Point out each leukocyte.
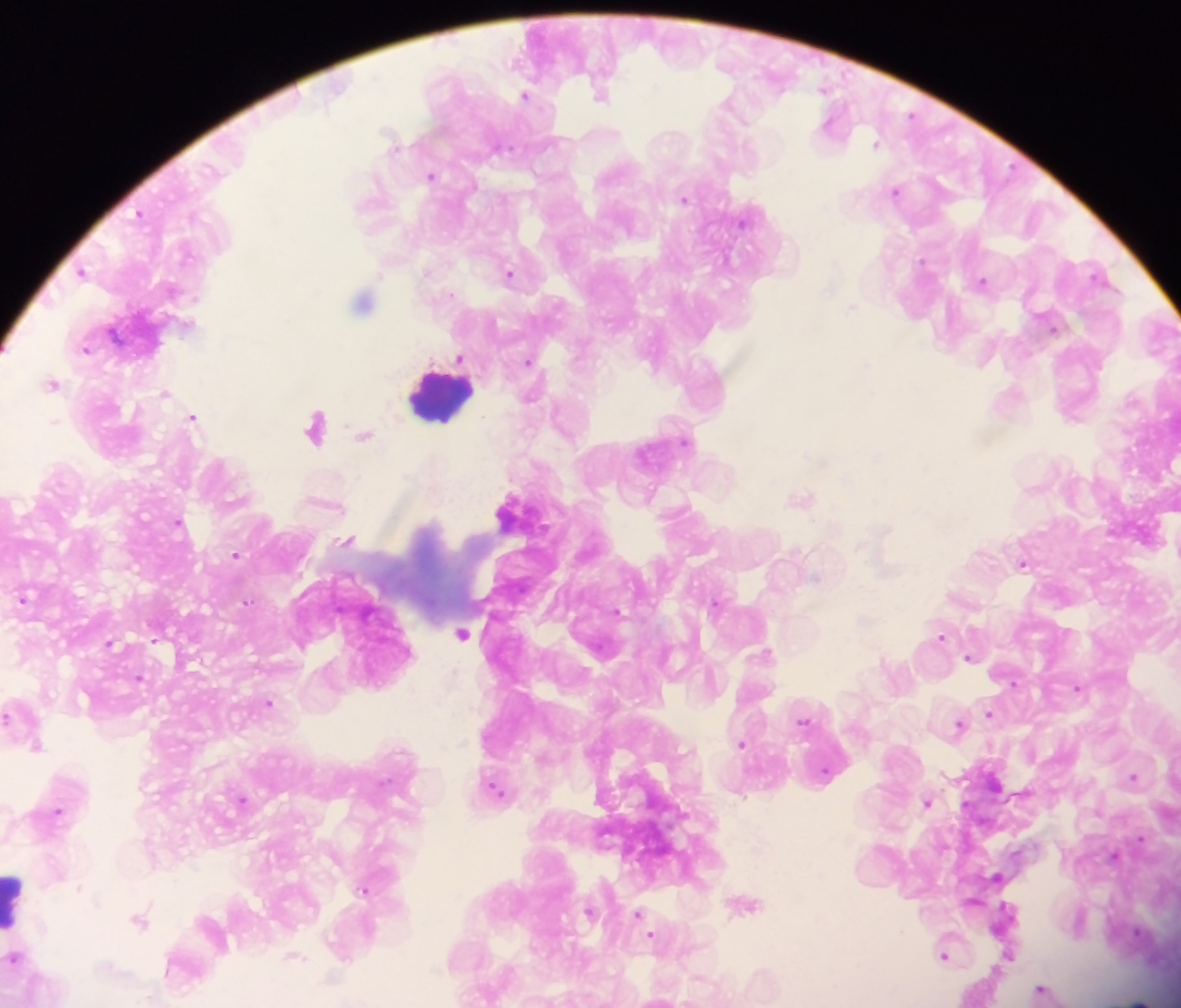

Approximate centers as {x, y} in pixels.
Leukocytes: {440, 395}, {16, 900}.

{
  "preparation": "thick blood film",
  "field_of_view": "single",
  "capture": "mobile-phone photograph through a microscope",
  "country": "Ghana",
  "image_size": "1181×1008 pixels",
  "plasmodium_parasite_locations": "approximate centers as {x, y} in pixels: {601, 94}, {526, 95}, {833, 124}, {877, 144}, {432, 176}, {897, 190}, {685, 198}, {83, 272}, {510, 274}, {983, 281}, {363, 302}, {852, 307}, {86, 349}, {461, 359}, {530, 360}, {54, 384}, {1010, 398}, {194, 417}, {317, 426}, {365, 435}, {802, 497}, {323, 502}, {515, 511}, {348, 540}, {236, 554}, {1024, 563}, {24, 599}, {717, 603}, {462, 632}, {941, 636}, {111, 643}, {971, 657}, {1079, 687}, {270, 703}, {991, 713}, {805, 720}, {961, 725}, {743, 743}, {38, 745}, {1135, 777}, {495, 788}, {243, 800}, {928, 802}, {58, 811}, {1116, 855}, {998, 876}, {365, 889}, {747, 904}, {590, 912}, {640, 916}, {140, 919}, {646, 925}, {946, 954}, {14, 958}, {186, 965}, {1043, 990}, {982, 991}, {1140, 1000}"
}